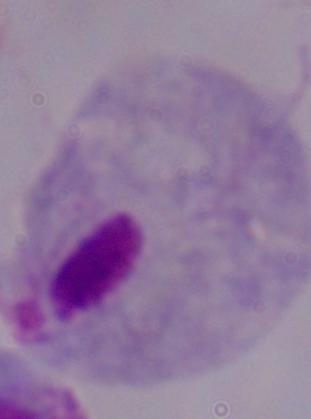

Summary:
  - Magnification: 1000x
  - Modality: photomicrograph
  - Identification: trichomonad